Classify this cell by malaria status.
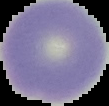
It is uninfected.

Summary:
  - Preparation: thin blood film
  - Image size: 109×106 pixels
  - Image type: cell region segmented out of the field of view; surrounding area masked to black